Assess this cell for malaria.
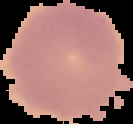
Uninfected.

preparation: thin blood smear
image_size: 133×124 pixels
image_type: cell region segmented out of the field of view; surrounding area masked to black